Comment on the morphology of the erythrocytes.
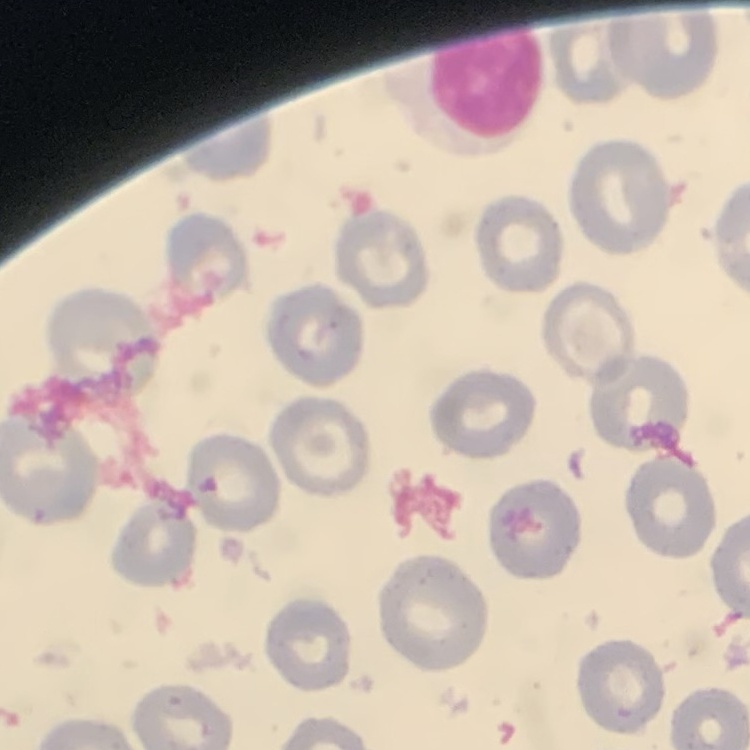

They show no rouleaux formation.

{
  "image_type": "square crop of a larger photomicrograph",
  "stain": "Field's or Giemsa",
  "preparation": "thin peripheral smear"
}